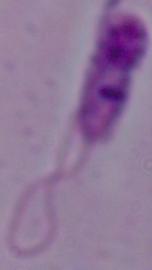
Summary:
  - Identification: Leishmania
  - Magnification: 1000x
  - Modality: photomicrograph